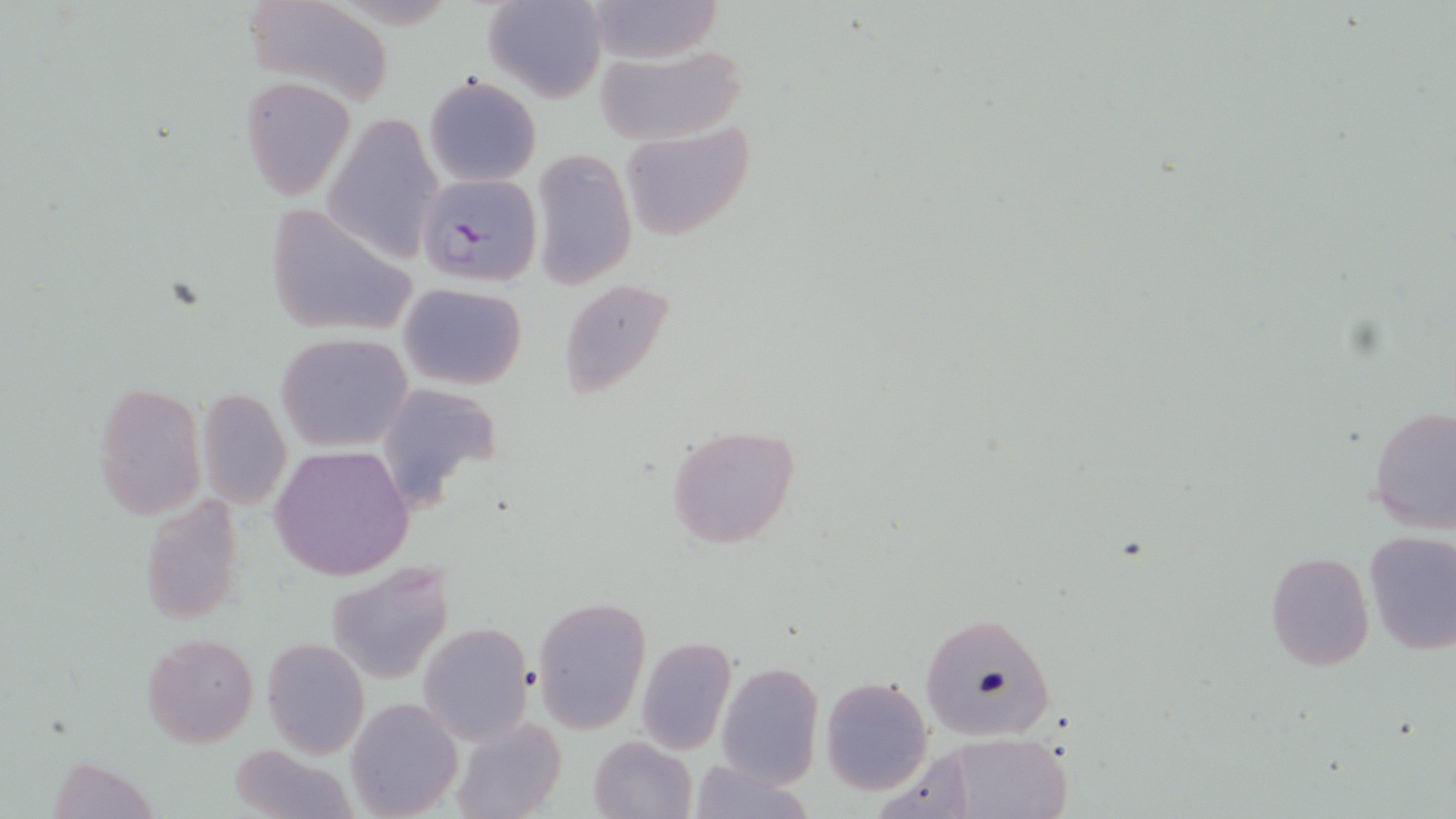
slide-level diagnosis = Plasmodium falciparum
stain = May-Grünwald-Giemsa
modality = light microscopy
field of view = one of a larger specimen
preparation = thin blood smear
uninfected red blood cell locations = approximate bounding boxes as (x1, y1, x2, y2) in pixels: (240, 0, 393, 103), (578, 0, 728, 65), (482, 1, 608, 102), (592, 43, 746, 146), (240, 75, 356, 202), (423, 75, 541, 187), (325, 112, 445, 262), (616, 122, 755, 242), (531, 146, 636, 290), (558, 278, 676, 403), (398, 282, 527, 388), (277, 333, 412, 452), (93, 381, 206, 518), (376, 384, 507, 508), (196, 388, 291, 509), (1366, 404, 1455, 533), (664, 422, 802, 550), (271, 444, 416, 581), (142, 497, 247, 626), (1362, 530, 1456, 656), (1264, 550, 1374, 672), (328, 562, 453, 683), (532, 596, 650, 734), (920, 609, 1059, 742), (417, 622, 535, 745), (141, 632, 257, 747), (636, 635, 738, 754), (262, 638, 370, 758), (717, 662, 825, 787), (821, 676, 933, 795), (346, 699, 463, 817), (450, 716, 566, 819), (944, 733, 1073, 818), (588, 734, 697, 819), (229, 744, 357, 819), (46, 756, 164, 818), (684, 756, 815, 819)
image size = 1456×819 pixels
magnification = 1000x
Plasmodium falciparum-infected red blood cell locations = approximate bounding boxes as (x1, y1, x2, y2) in pixels: (416, 172, 544, 287)